Assess the morphology of the erythrocytes.
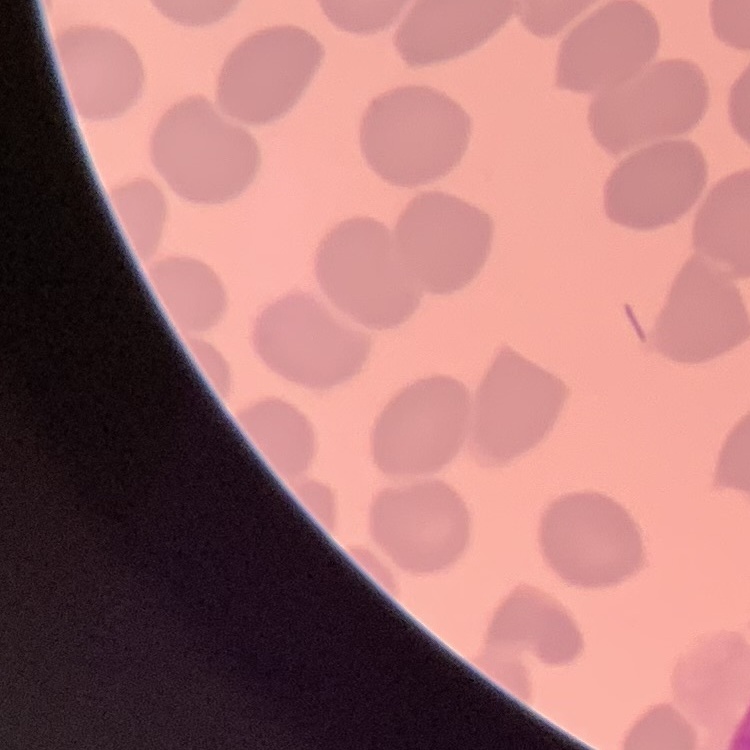
No rouleaux formation.

Summary:
  - Stain: Field's or Giemsa
  - Image type: one tile cut from a larger photomicrograph
  - Preparation: thin peripheral smear